Report the malaria status of this cell.
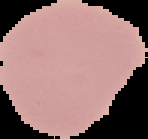
It is uninfected.

{
  "image_type": "cell region segmented out of the field of view; surrounding area masked to black",
  "image_size": "148×139 pixels",
  "preparation": "thin blood smear"
}